Report the malaria status of this cell.
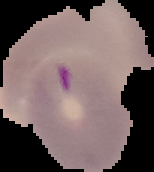

It is parasitized.

image_type: segmented cell region with the area outside set to black
image_size: 154×172 pixels
preparation: thin blood film